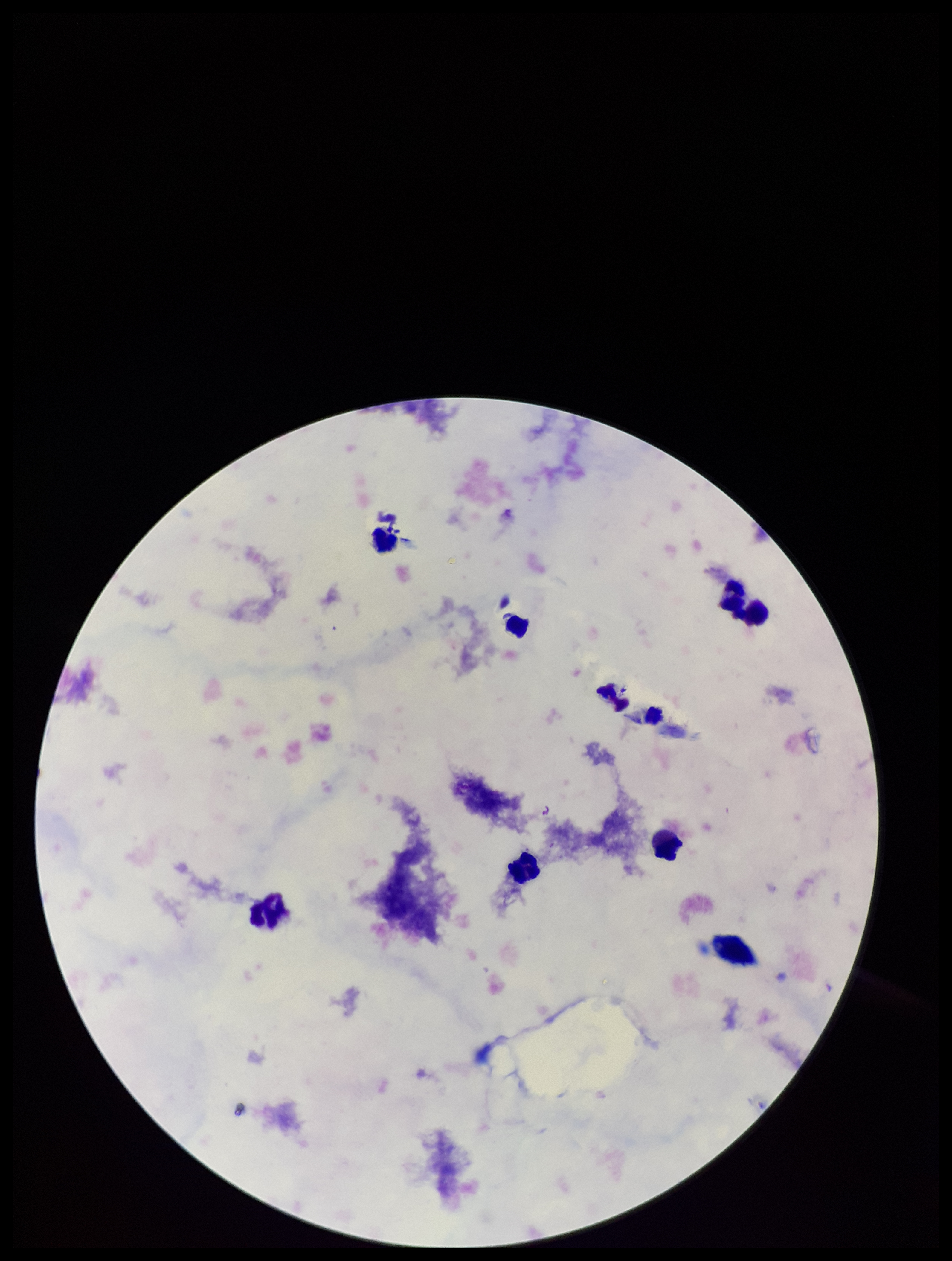

Summary:
  - Preparation: thick
  - Leukocyte count: 8
  - Stain: Giemsa
  - Field of view: single
  - Plasmodium parasites: none identified
  - Capture: smartphone photograph through the microscope eyepiece
  - Parasite count: 0
  - Image size: 952×1261 pixels
  - Patient malaria status: negative